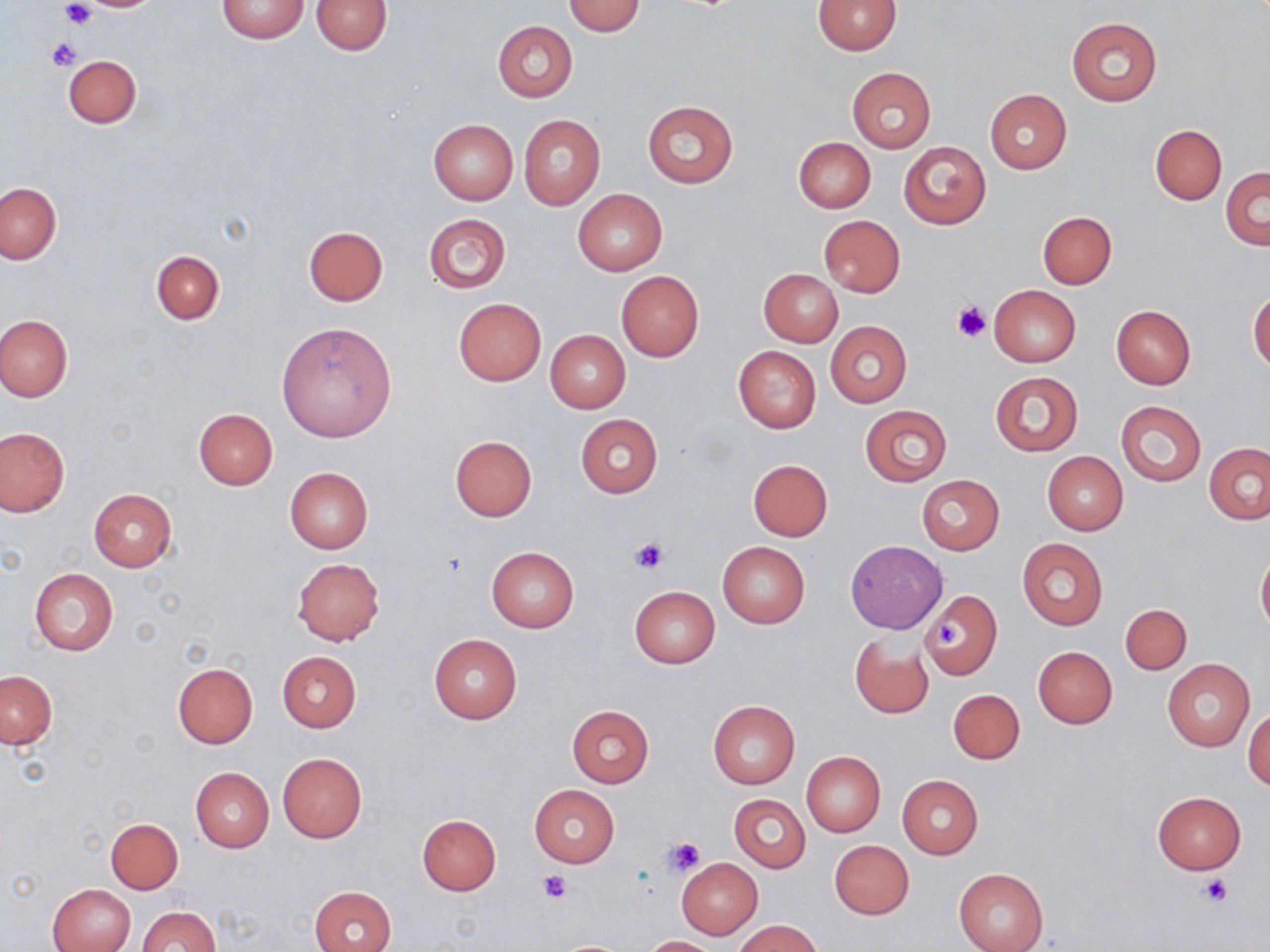

{
  "slide_level_diagnosis": "no evidence of blood parasites",
  "field_of_view": "one of a larger specimen",
  "image_size": "1270×952 pixels",
  "modality": "light microscopy",
  "magnification": "1000x",
  "preparation": "thin blood smear",
  "platelet_locations": "approximate bounding boxes as [x1, y1, x2, y2] in pixels: [58, 2, 97, 30], [46, 37, 83, 71], [951, 301, 993, 343], [629, 535, 670, 575], [935, 619, 966, 650], [664, 835, 705, 874], [538, 869, 572, 902], [1201, 874, 1231, 906]",
  "uninfected_red_blood_cell_locations": "approximate bounding boxes as [x1, y1, x2, y2] in pixels: [215, 0, 311, 44], [312, 0, 392, 55], [561, 0, 646, 36], [813, 0, 901, 55], [1067, 16, 1162, 105], [492, 20, 578, 102], [62, 54, 141, 128], [846, 67, 935, 153], [985, 89, 1072, 173], [641, 101, 739, 189], [519, 114, 604, 210], [429, 121, 517, 204], [1150, 124, 1226, 204], [793, 137, 875, 214], [898, 141, 991, 229], [1221, 167, 1269, 250], [0, 183, 62, 263], [573, 189, 667, 276], [1036, 211, 1116, 289], [423, 214, 511, 293], [819, 215, 905, 297], [304, 226, 388, 306], [151, 250, 224, 324], [758, 269, 842, 347], [616, 271, 704, 362], [989, 285, 1081, 367], [1249, 287, 1270, 371], [453, 298, 546, 387], [1111, 305, 1196, 389], [0, 314, 72, 401], [277, 321, 397, 442], [825, 321, 913, 407], [545, 330, 630, 413], [733, 345, 822, 434], [989, 371, 1083, 454], [1116, 401, 1206, 485], [859, 405, 952, 484], [193, 408, 278, 489], [575, 413, 663, 497], [0, 428, 69, 516], [449, 436, 537, 520], [1204, 443, 1270, 524], [1042, 452, 1127, 535], [748, 459, 833, 540], [285, 467, 373, 552], [916, 474, 1004, 554], [87, 488, 177, 572], [1017, 537, 1108, 630], [845, 541, 946, 633], [718, 542, 810, 627], [486, 547, 578, 632], [1256, 547, 1270, 635], [292, 559, 385, 645], [29, 568, 118, 654], [629, 586, 719, 668], [919, 588, 1002, 681], [1120, 604, 1191, 674], [429, 633, 522, 723], [849, 633, 933, 718], [1033, 646, 1117, 728], [277, 652, 362, 732], [1162, 658, 1254, 751], [172, 662, 259, 748], [2, 670, 56, 749], [949, 689, 1024, 764], [708, 701, 800, 789], [566, 705, 653, 788], [1244, 707, 1270, 791], [801, 751, 886, 835], [277, 752, 366, 844], [191, 768, 274, 853], [897, 775, 983, 859], [529, 785, 618, 868], [1151, 790, 1248, 875], [729, 794, 810, 872], [417, 814, 501, 895], [107, 818, 183, 893], [830, 840, 914, 919], [677, 858, 762, 939], [953, 869, 1049, 952], [48, 883, 135, 951], [309, 886, 395, 952], [138, 905, 220, 952], [736, 920, 820, 952], [644, 935, 718, 951]",
  "stain": "May-Grünwald-Giemsa"
}